Name the parasite shown.
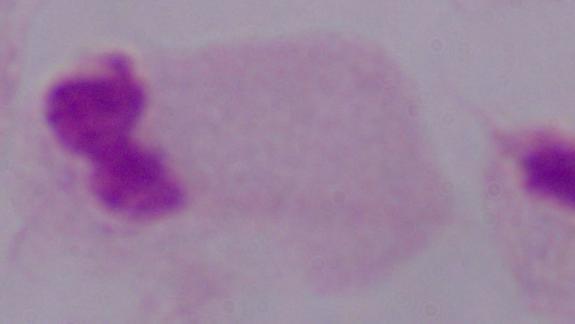
A trichomonad.

Micrograph. 1000x magnification.